Assess this cell for malaria.
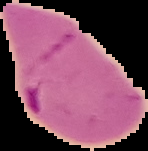
Parasitized.

Cell region segmented out of the field of view; the surrounding area is masked to black. Image is 148×151 pixels. From a thin blood smear.